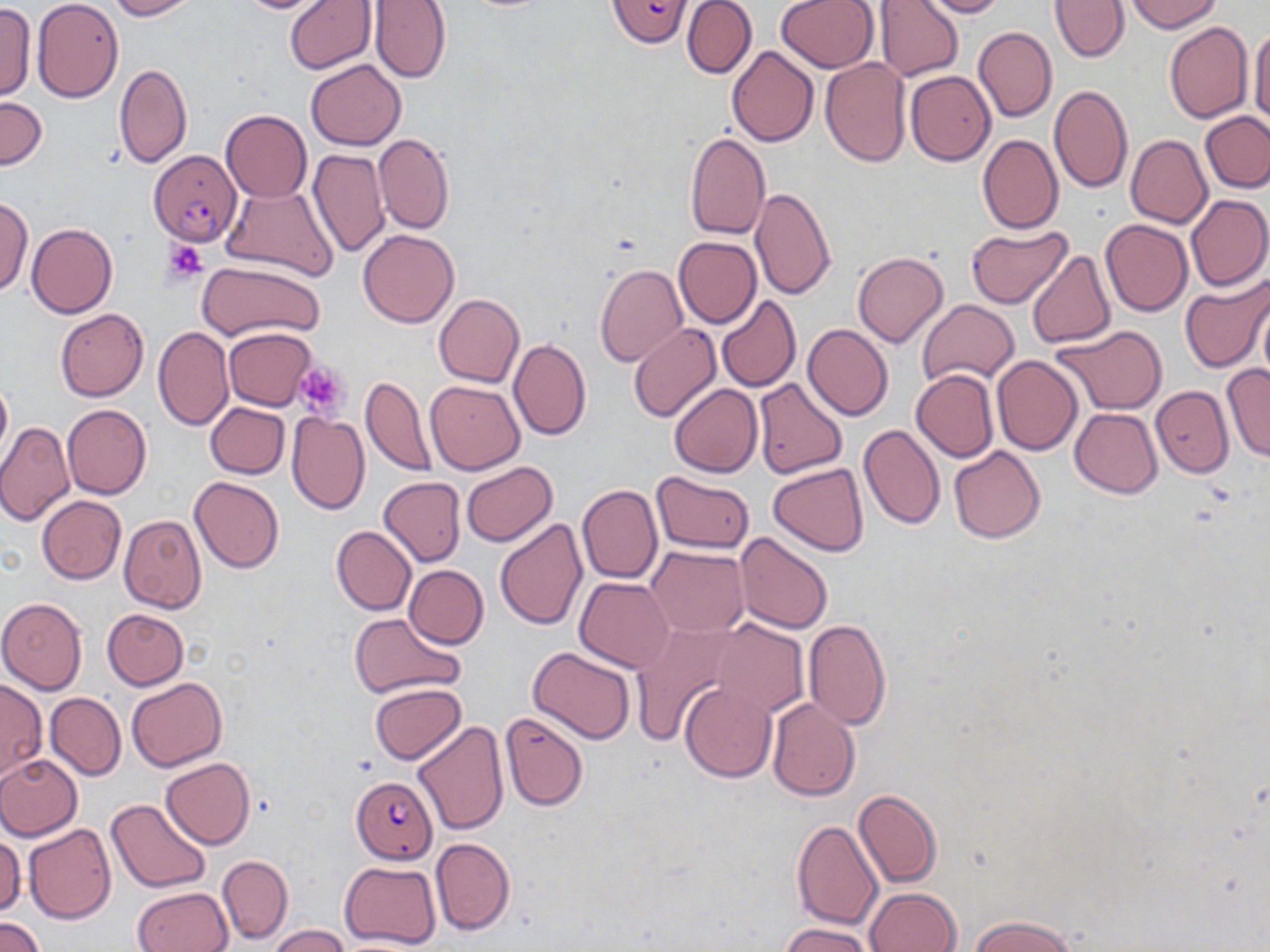
{
  "plasmodium_falciparum_infected_red_blood_cell_locations": "approximate bounding boxes as [x1, y1, x2, y2] in pixels: [606, 0, 693, 47], [148, 150, 242, 245], [350, 775, 437, 861]",
  "slide_level_diagnosis": "Plasmodium falciparum",
  "stain": "May-Grünwald-Giemsa",
  "uninfected_red_blood_cell_locations": "approximate bounding boxes as [x1, y1, x2, y2] in pixels: [104, 0, 198, 20], [229, 0, 336, 14], [284, 0, 376, 73], [294, 0, 384, 139], [682, 0, 757, 79], [776, 0, 879, 72], [874, 0, 963, 82], [916, 0, 1007, 18], [1050, 0, 1130, 62], [1127, 0, 1221, 33], [31, 1, 124, 102], [368, 1, 450, 83], [0, 3, 36, 100], [1165, 22, 1254, 124], [1249, 22, 1270, 129], [972, 26, 1057, 122], [725, 46, 819, 148], [306, 59, 406, 151], [820, 59, 911, 168], [114, 64, 192, 168], [905, 71, 995, 166], [1049, 85, 1132, 192], [0, 96, 48, 170], [221, 110, 312, 202], [1198, 111, 1270, 194], [684, 132, 770, 241], [373, 133, 455, 235], [977, 134, 1064, 234], [1125, 136, 1212, 228], [308, 149, 390, 258], [221, 184, 339, 283], [750, 187, 836, 300], [1186, 194, 1269, 292], [1, 195, 34, 295], [1100, 218, 1192, 315], [26, 223, 116, 318], [966, 226, 1072, 308], [359, 230, 458, 328], [674, 237, 761, 328], [1027, 249, 1116, 348], [852, 252, 947, 348], [198, 258, 327, 341], [595, 263, 688, 367], [1179, 277, 1270, 375], [1257, 294, 1270, 392], [434, 295, 525, 387], [716, 295, 801, 393], [916, 299, 1018, 388], [55, 307, 149, 401], [628, 323, 721, 423], [802, 324, 893, 421], [1050, 325, 1168, 416], [153, 326, 234, 431], [224, 328, 318, 411], [508, 338, 591, 441], [991, 356, 1082, 455], [1221, 363, 1270, 462], [912, 369, 998, 463], [360, 375, 435, 478], [0, 376, 10, 466], [753, 378, 847, 480], [426, 381, 523, 474], [670, 384, 762, 478], [1151, 385, 1233, 478], [204, 403, 289, 478], [63, 404, 151, 499], [1070, 407, 1162, 498], [287, 413, 368, 515], [0, 420, 75, 525], [858, 423, 945, 529], [948, 446, 1046, 543], [461, 461, 558, 547], [769, 464, 869, 557], [652, 472, 755, 553], [190, 476, 284, 573], [377, 477, 466, 566], [577, 485, 663, 584], [37, 495, 126, 583], [118, 514, 207, 614], [495, 517, 589, 631], [331, 526, 415, 615], [733, 532, 833, 634], [645, 546, 748, 637], [404, 565, 489, 649], [575, 577, 675, 672], [551, 586, 661, 735], [0, 597, 87, 694], [102, 609, 188, 689], [349, 612, 465, 699], [803, 619, 891, 730], [713, 621, 808, 718], [630, 624, 741, 742], [527, 646, 635, 743], [0, 677, 47, 782], [126, 678, 228, 772], [369, 682, 466, 764], [680, 682, 777, 781], [45, 693, 125, 779], [767, 698, 860, 802], [500, 712, 589, 810], [413, 720, 509, 837], [0, 754, 83, 841], [161, 757, 256, 850], [852, 789, 941, 888], [105, 799, 211, 894], [792, 821, 883, 932], [23, 823, 115, 925], [0, 836, 25, 915], [431, 839, 515, 934], [217, 854, 292, 945], [340, 860, 441, 950], [133, 887, 233, 951], [866, 888, 962, 952], [971, 915, 1076, 952], [1, 916, 45, 952], [779, 922, 878, 952], [270, 924, 350, 952]",
  "magnification": "1000x",
  "preparation": "thin blood smear",
  "modality": "light microscopy",
  "platelet_locations": "approximate bounding boxes as [x1, y1, x2, y2] in pixels: [162, 240, 209, 285], [294, 362, 351, 418]",
  "field_of_view": "single",
  "image_size": "1270×952 pixels"
}